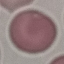
Malaria status: uninfected. Cell patch, automatically extracted from a larger field of view and resized to 64 × 64 pixels. Photographed with a smartphone camera at the microscope eyepiece. Thin blood film. Giemsa stain.